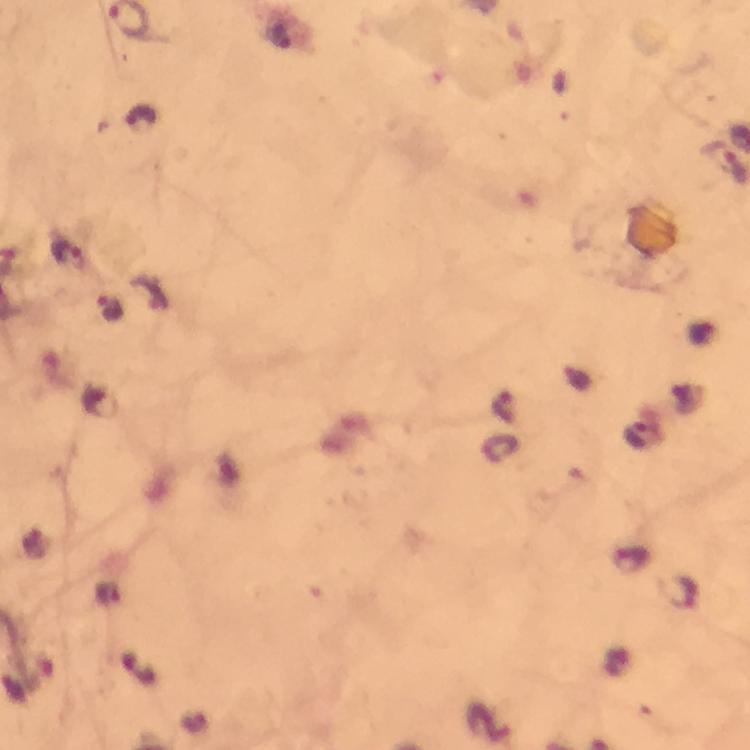
Approximate centers as {x, y} in pixels. Malaria parasite locations: {68, 255}, {110, 308}, {638, 439}, {683, 597}. Image is 750×750 pixels. Photographed with a smartphone mounted on the microscope. From a malaria diagnostic workup. Thick blood smear. Giemsa stain. A crop from one field of view. 100x magnification. Immersion oil was used.